Classify this cell by malaria status.
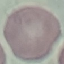
Uninfected.

Summary:
  - Stain: Giemsa
  - Image type: cell patch, automatically extracted from a larger field of view and resized to 64 × 64 pixels
  - Capture: smartphone camera at the microscope eyepiece
  - Preparation: thin blood smear